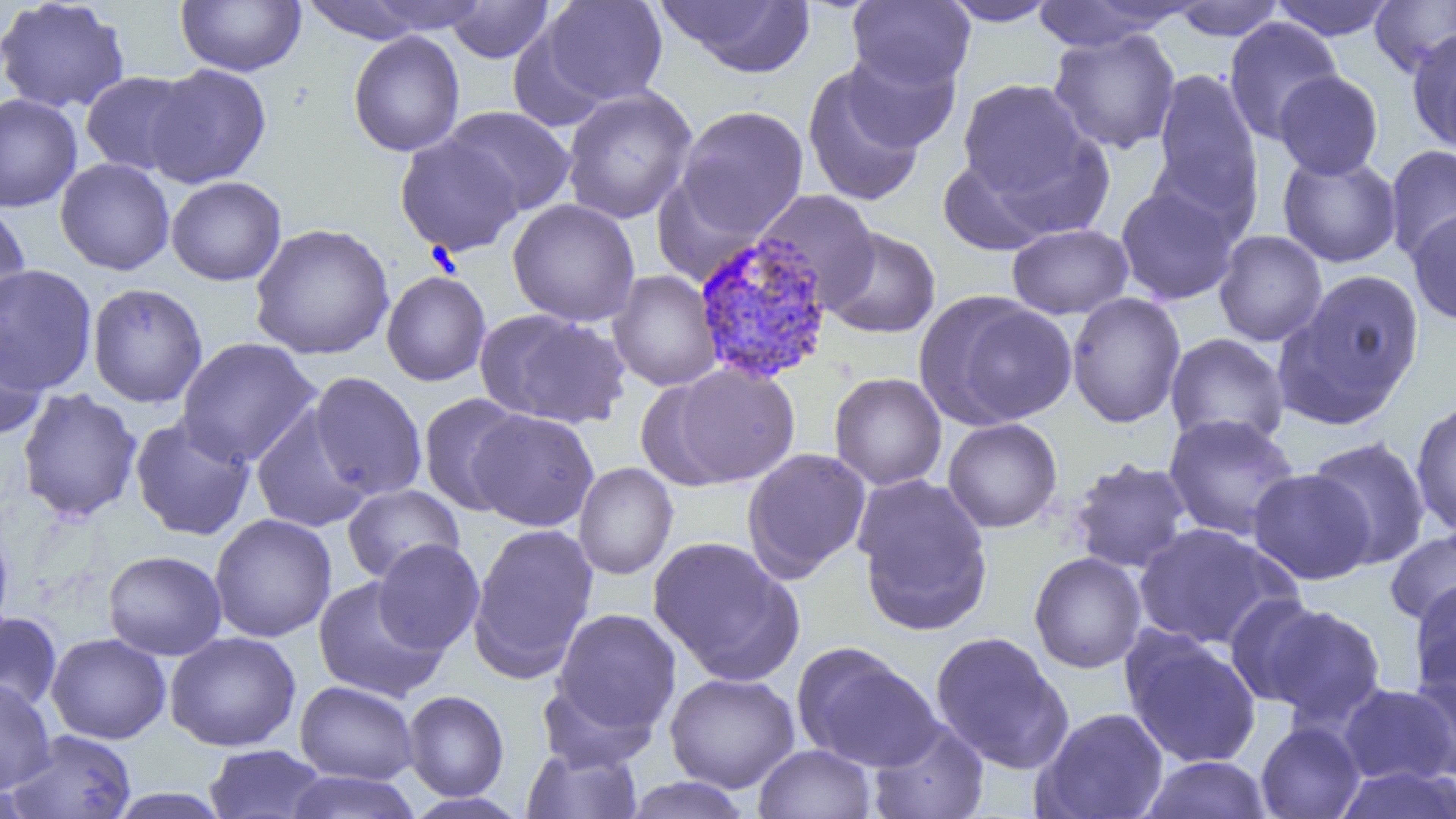
slide-level diagnosis = Plasmodium vivax
uninfected red blood cell locations = approximate bounding boxes as [x1, y1, x2, y2] in pixels: [0, 0, 131, 114], [175, 0, 306, 77], [352, 0, 494, 36], [541, 0, 667, 106], [656, 0, 816, 78], [940, 0, 1061, 27], [1029, 0, 1192, 51], [1269, 0, 1398, 41], [1369, 0, 1456, 77], [296, 1, 441, 43], [444, 1, 555, 63], [847, 1, 975, 90], [1168, 1, 1286, 41], [1223, 17, 1344, 144], [1047, 28, 1182, 154], [1407, 28, 1456, 153], [348, 30, 466, 157], [842, 49, 961, 153], [143, 63, 272, 189], [802, 65, 926, 207], [1150, 68, 1262, 217], [80, 71, 197, 176], [1273, 71, 1384, 179], [957, 78, 1094, 203], [560, 86, 698, 225], [0, 93, 83, 212], [674, 105, 810, 239], [441, 106, 576, 217], [394, 133, 525, 257], [1384, 144, 1456, 263], [1277, 151, 1402, 268], [937, 154, 1056, 257], [54, 158, 175, 275], [165, 176, 287, 286], [1115, 185, 1240, 305], [753, 189, 881, 307], [506, 198, 641, 327], [0, 200, 32, 324], [1407, 210, 1456, 326], [249, 223, 395, 360], [1007, 223, 1133, 319], [821, 227, 941, 339], [1214, 230, 1327, 346], [0, 263, 98, 396], [608, 269, 724, 391], [1280, 269, 1424, 422], [381, 270, 492, 386], [87, 282, 208, 408], [915, 292, 1076, 430], [1066, 292, 1186, 428], [475, 307, 631, 430], [0, 322, 48, 441], [1165, 333, 1290, 449], [176, 337, 322, 467], [659, 362, 802, 488], [309, 371, 426, 500], [828, 372, 947, 491], [16, 387, 143, 523], [416, 393, 529, 516], [1410, 399, 1456, 537], [251, 407, 372, 533], [468, 408, 600, 531], [1163, 413, 1301, 542], [129, 415, 257, 541], [942, 418, 1063, 533], [1306, 435, 1431, 569], [741, 447, 872, 582], [1068, 457, 1193, 573], [573, 462, 678, 580], [1248, 468, 1375, 584], [852, 474, 994, 635], [342, 484, 464, 584], [209, 513, 337, 642], [0, 518, 15, 649], [468, 523, 599, 680], [1132, 523, 1292, 650], [1384, 528, 1456, 627], [648, 534, 803, 683], [373, 538, 485, 654], [102, 549, 227, 660], [1029, 552, 1147, 673], [312, 576, 449, 703], [1408, 580, 1456, 701], [1225, 594, 1332, 708], [1256, 602, 1387, 727], [551, 608, 682, 735], [0, 611, 63, 715], [164, 631, 301, 751], [930, 631, 1072, 773], [1122, 631, 1262, 768], [46, 633, 171, 744], [792, 641, 941, 771], [664, 672, 800, 793], [1404, 675, 1456, 783], [0, 678, 56, 795], [536, 678, 657, 772], [295, 680, 419, 784], [1338, 683, 1454, 786], [402, 690, 510, 801], [1033, 707, 1169, 819], [868, 719, 989, 819], [1255, 721, 1366, 819], [6, 729, 138, 819], [754, 743, 876, 819], [203, 744, 328, 819], [522, 745, 643, 818], [1140, 755, 1273, 818], [1331, 764, 1456, 819], [283, 771, 421, 819], [620, 776, 753, 819], [104, 788, 233, 818], [402, 792, 532, 818]
field of view = single
modality = optical microscopy
magnification = 1000x
preparation = thin blood smear
Plasmodium vivax-infected red blood cell locations = approximate bounding boxes as [x1, y1, x2, y2] in pixels: [692, 231, 835, 386]
image size = 1456×819 pixels